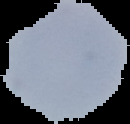
Summary:
  - Malaria status: uninfected
  - Image size: 130×124 pixels
  - Image type: segmented cell region on a black background
  - Preparation: thin blood smear